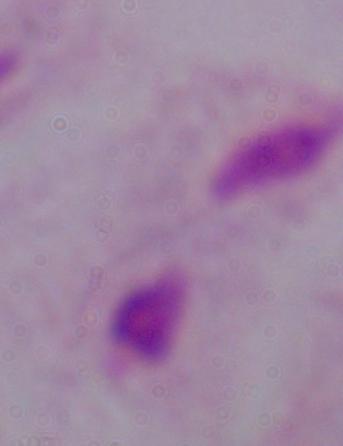

Summary:
  - Magnification: 1000x
  - Identification: trichomonad
  - Modality: photomicrograph